Comment on the morphology of the red blood cells.
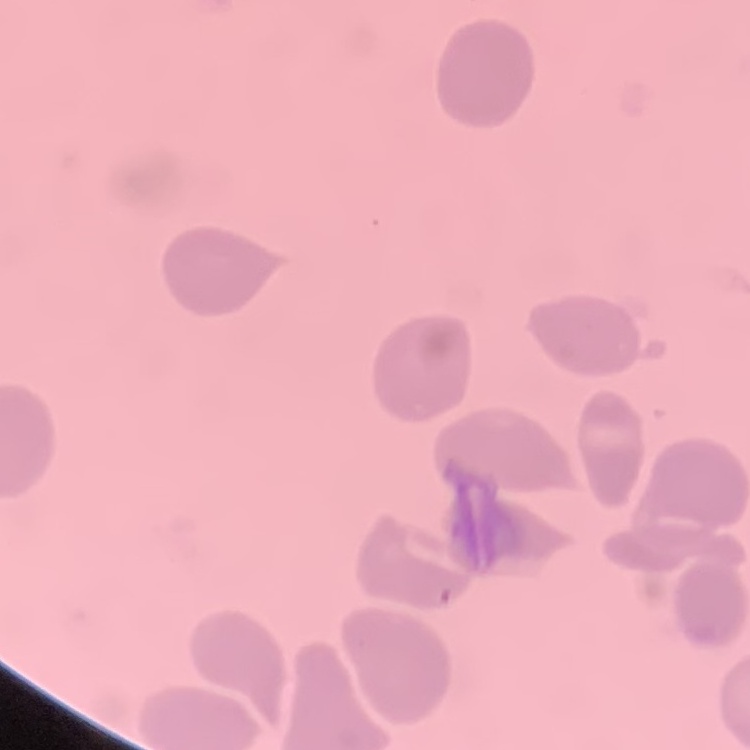
They show no rouleaux formation.

image type = one tile cut from a larger photomicrograph
stain = Field's or Giemsa
preparation = thin blood film